Locate every blood parasite and identify its species.
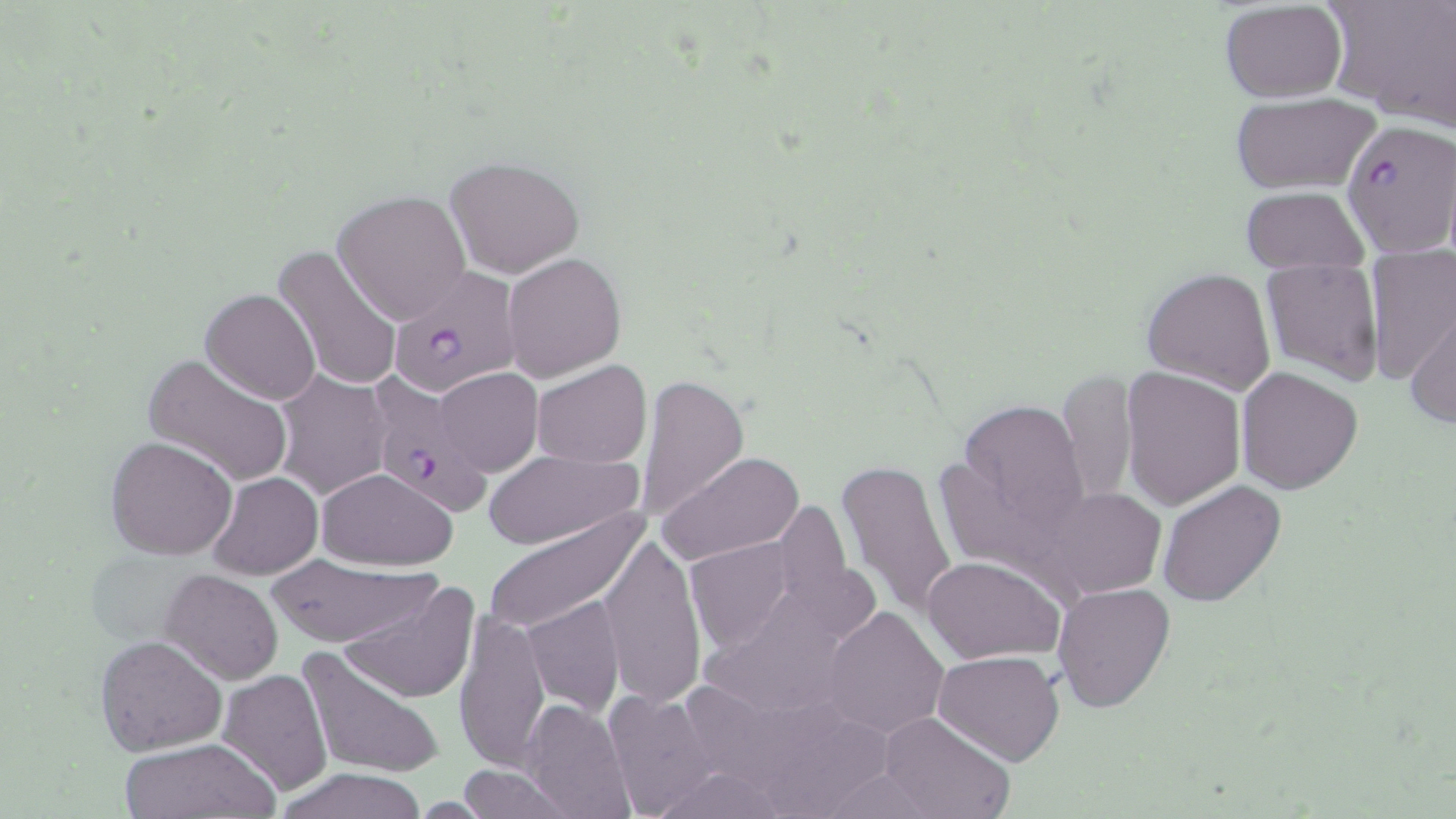

Approximate bounding boxes as (x1, y1, x2, y2) in pixels.
Plasmodium falciparum-infected red blood cells: (1344, 119, 1456, 254), (386, 267, 521, 396), (375, 371, 488, 517).
No Plasmodium ovale, Plasmodium malariae, Plasmodium vivax, Babesia divergens, or Trypanosoma brucei observed.

Summary:
  - Uninfected red blood cell locations: (1328, 0, 1456, 132), (1219, 2, 1347, 103), (1227, 94, 1379, 197), (444, 155, 586, 278), (1238, 188, 1369, 271), (334, 189, 472, 325), (274, 245, 402, 395), (503, 253, 626, 382), (1364, 254, 1456, 383), (1260, 262, 1383, 384), (1141, 267, 1277, 394), (200, 288, 322, 405), (1407, 310, 1456, 431), (142, 352, 296, 488), (532, 358, 652, 467), (433, 367, 542, 477), (1122, 367, 1247, 509), (1236, 367, 1364, 494), (1058, 368, 1139, 507), (273, 369, 392, 500), (634, 373, 748, 522), (956, 398, 1091, 543), (104, 435, 237, 559), (483, 449, 641, 550), (659, 451, 805, 566), (835, 458, 959, 620), (316, 467, 456, 571), (207, 470, 322, 579), (1159, 480, 1287, 607), (1043, 487, 1166, 598), (480, 508, 646, 635), (597, 532, 706, 709), (685, 536, 797, 656), (922, 554, 1065, 664), (262, 555, 438, 649), (161, 568, 284, 684), (336, 579, 480, 704), (1052, 583, 1176, 713), (522, 596, 625, 715), (822, 606, 948, 739), (452, 611, 553, 772), (95, 635, 226, 755), (298, 646, 445, 782), (934, 650, 1063, 767), (217, 668, 334, 797), (600, 689, 724, 816), (518, 698, 635, 819), (879, 711, 1013, 819), (117, 737, 279, 817), (455, 764, 578, 818), (274, 767, 431, 819), (646, 767, 791, 818)
  - Slide-level diagnosis: Plasmodium falciparum
  - Modality: light microscopy
  - Stain: May-Grünwald-Giemsa
  - Field of view: single
  - Preparation: thin blood film
  - Magnification: 1000x
  - Image size: 1456×819 pixels